Locate every Plasmodium parasite and every leukocyte.
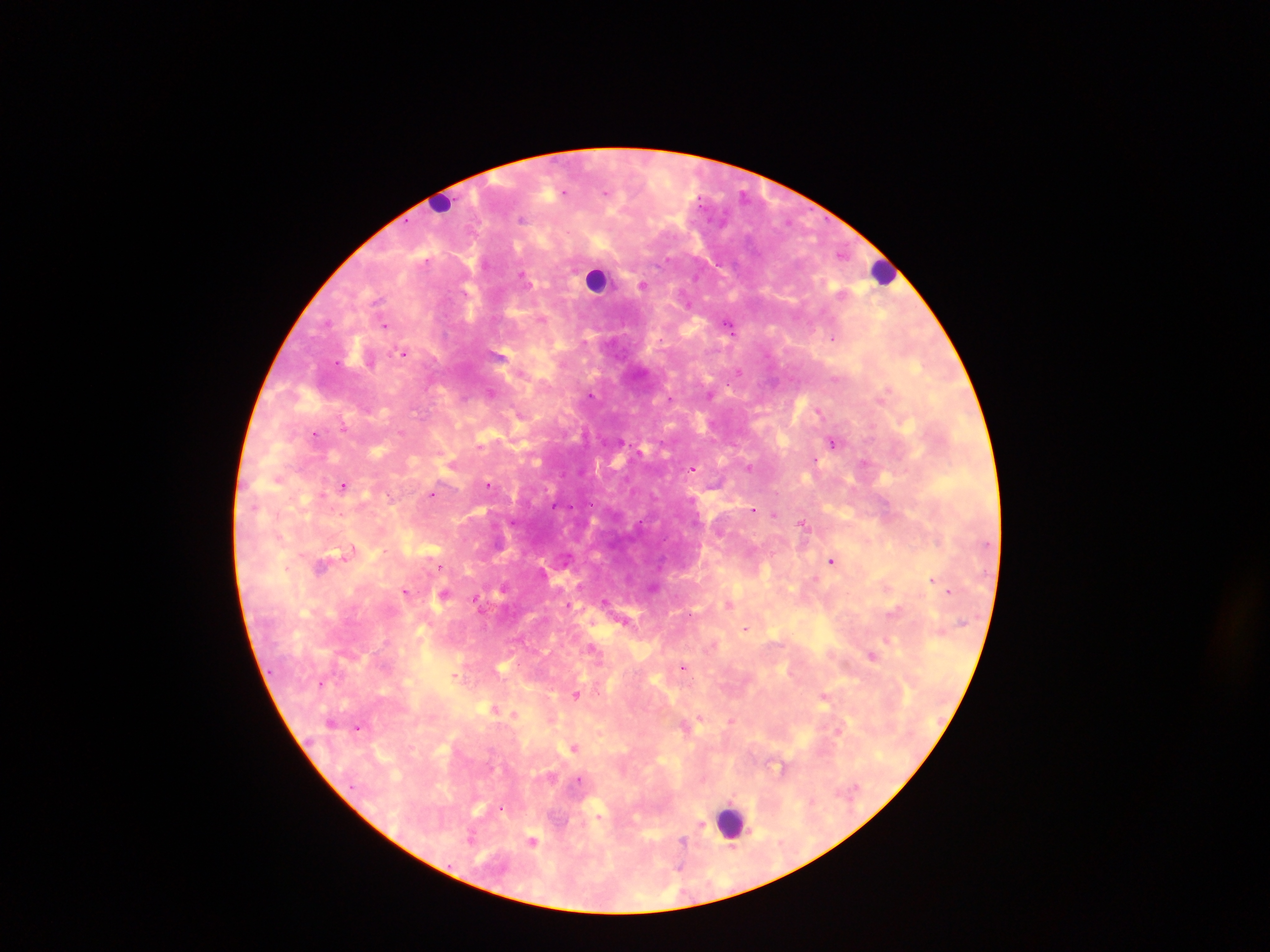

Approximate centers as (x, y) in pixels.
Plasmodium parasites: (563, 193), (698, 203), (521, 219), (642, 285), (329, 322), (728, 323), (385, 324), (833, 339), (404, 353), (739, 372), (887, 389), (491, 393), (593, 394), (710, 394), (468, 399), (821, 412), (345, 427), (315, 434), (833, 440), (620, 442), (815, 459), (864, 462), (749, 466), (694, 469), (278, 480), (489, 484), (344, 486), (432, 494), (754, 510), (775, 513), (803, 522), (832, 560), (441, 566), (932, 579), (502, 588), (949, 591), (406, 592), (444, 593), (476, 599), (606, 600), (746, 629), (593, 648), (684, 667), (455, 675), (577, 693), (359, 729), (575, 747), (576, 780), (352, 787), (502, 809), (703, 824), (685, 842), (681, 863), (448, 865).
Leukocytes: (447, 204), (886, 271), (595, 280), (731, 825).

Summary:
  - Capture: mobile-phone photograph through a microscope
  - Preparation: thick blood smear
  - Image size: 1270×952 pixels
  - Field of view: single
  - Country: Ghana